Classify this cell by malaria status.
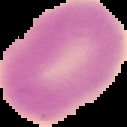
Uninfected.

Summary:
  - Image type: segmented cell region with the area outside set to black
  - Image size: 127×127 pixels
  - Preparation: thin blood film